Assess the morphology of the erythrocytes.
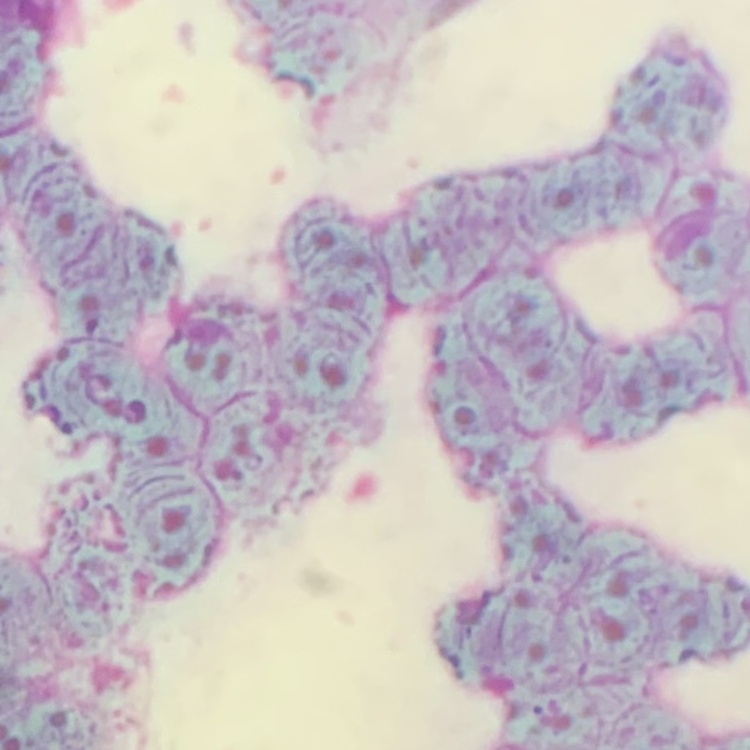
Rouleaux formation.

preparation = thin blood smear
image type = one tile cut from a larger photomicrograph
stain = Field's or Giemsa